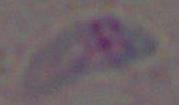

Summary:
  - Modality: photomicrograph
  - Identification: Toxoplasma gondii
  - Magnification: 1000x